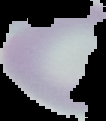

Summary:
  - Preparation: thin blood smear
  - Image type: segmented cell region on a black background
  - Image size: 106×121 pixels
  - Result: negative for Plasmodium parasites